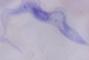

Summary:
  - Identification: trypanosome
  - Modality: photomicrograph
  - Magnification: 1000x